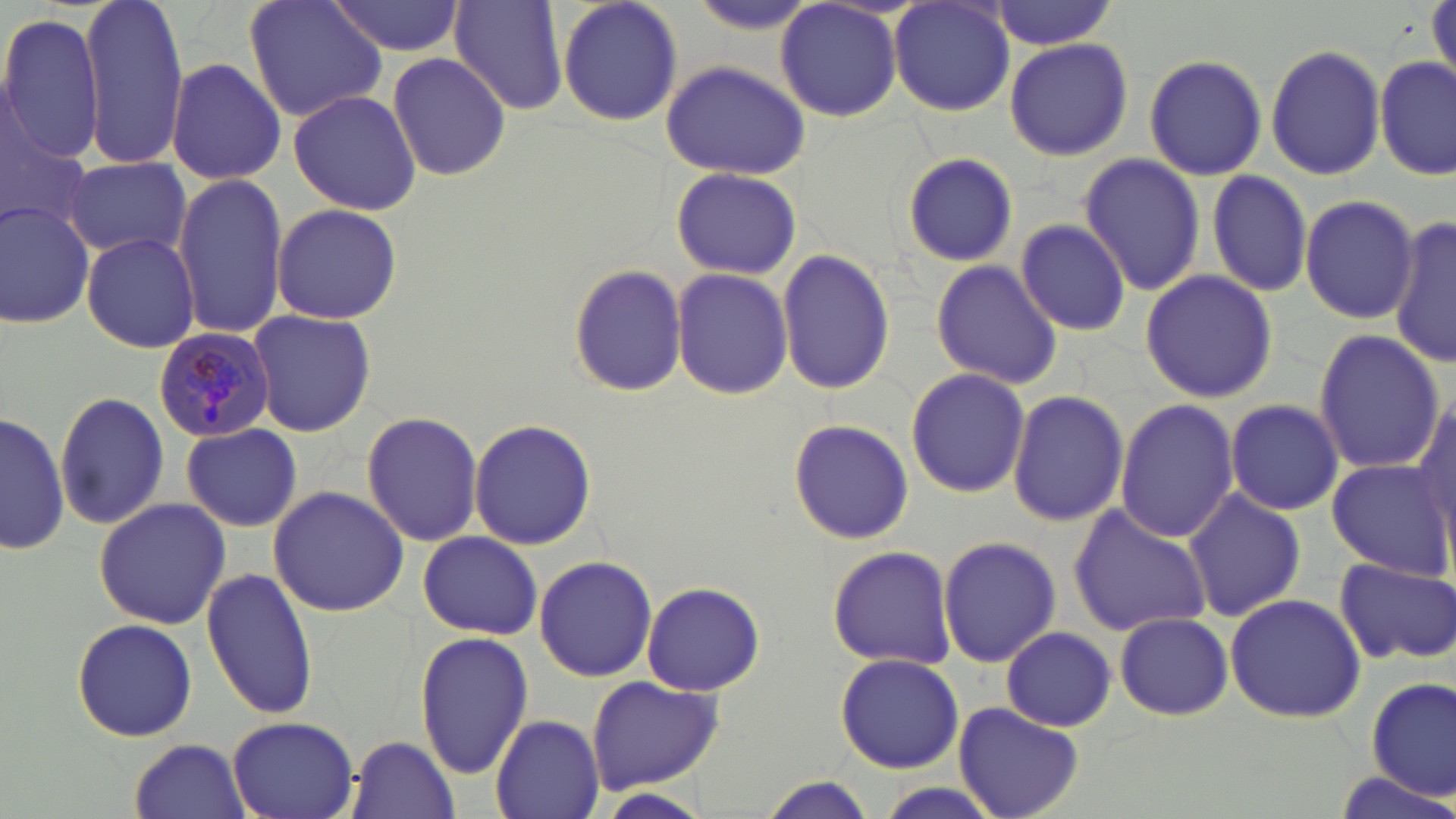

Plasmodium malariae-infected red blood cell locations = approximate bounding boxes as [x1, y1, x2, y2] in pixels: [152, 327, 274, 443]
slide-level diagnosis = Plasmodium malariae
modality = optical microscopy
preparation = thin blood smear
stain = May-Grünwald-Giemsa
uninfected red blood cell locations = approximate bounding boxes as [x1, y1, x2, y2] in pixels: [78, 0, 187, 171], [244, 0, 389, 122], [327, 0, 466, 58], [448, 0, 571, 118], [556, 0, 685, 128], [986, 0, 1122, 50], [1426, 0, 1456, 88], [774, 1, 904, 122], [888, 2, 1016, 117], [0, 11, 107, 166], [1004, 35, 1132, 162], [1264, 43, 1385, 181], [387, 52, 512, 180], [1144, 52, 1269, 181], [1376, 55, 1452, 181], [164, 58, 287, 184], [660, 60, 810, 179], [286, 90, 421, 215], [0, 109, 92, 232], [901, 149, 1021, 265], [1077, 154, 1207, 295], [64, 156, 191, 262], [669, 165, 801, 278], [1206, 169, 1314, 298], [171, 173, 289, 338], [1299, 195, 1420, 323], [0, 199, 96, 328], [270, 204, 402, 323], [1015, 216, 1132, 337], [1389, 218, 1456, 367], [80, 233, 199, 353], [776, 247, 896, 397], [930, 260, 1064, 391], [566, 264, 689, 397], [671, 268, 795, 399], [1139, 269, 1278, 403], [248, 309, 375, 437], [1312, 330, 1444, 474], [905, 367, 1031, 499], [1007, 387, 1130, 527], [54, 388, 171, 532], [1409, 390, 1455, 553], [1224, 398, 1345, 516], [1114, 399, 1240, 545], [1, 410, 70, 555], [358, 410, 485, 546], [786, 418, 915, 545], [470, 419, 596, 549], [182, 425, 301, 531], [1325, 458, 1450, 578], [268, 485, 409, 615], [1182, 487, 1306, 622], [92, 497, 231, 630], [1066, 501, 1213, 639], [416, 530, 542, 639], [937, 534, 1062, 668], [825, 544, 957, 670], [534, 555, 658, 682], [1335, 555, 1456, 667], [201, 566, 320, 720], [641, 582, 765, 694], [1224, 592, 1366, 723], [1113, 612, 1234, 720], [71, 616, 197, 742], [1001, 626, 1117, 731], [415, 629, 534, 781], [835, 651, 964, 773], [586, 675, 726, 791], [1365, 677, 1455, 801], [954, 702, 1084, 819], [489, 715, 604, 819], [227, 716, 359, 818], [346, 734, 459, 819], [129, 738, 253, 818], [1331, 770, 1455, 818], [755, 777, 879, 819]
image size = 1456×819 pixels
field of view = one of a larger specimen
magnification = 1000x